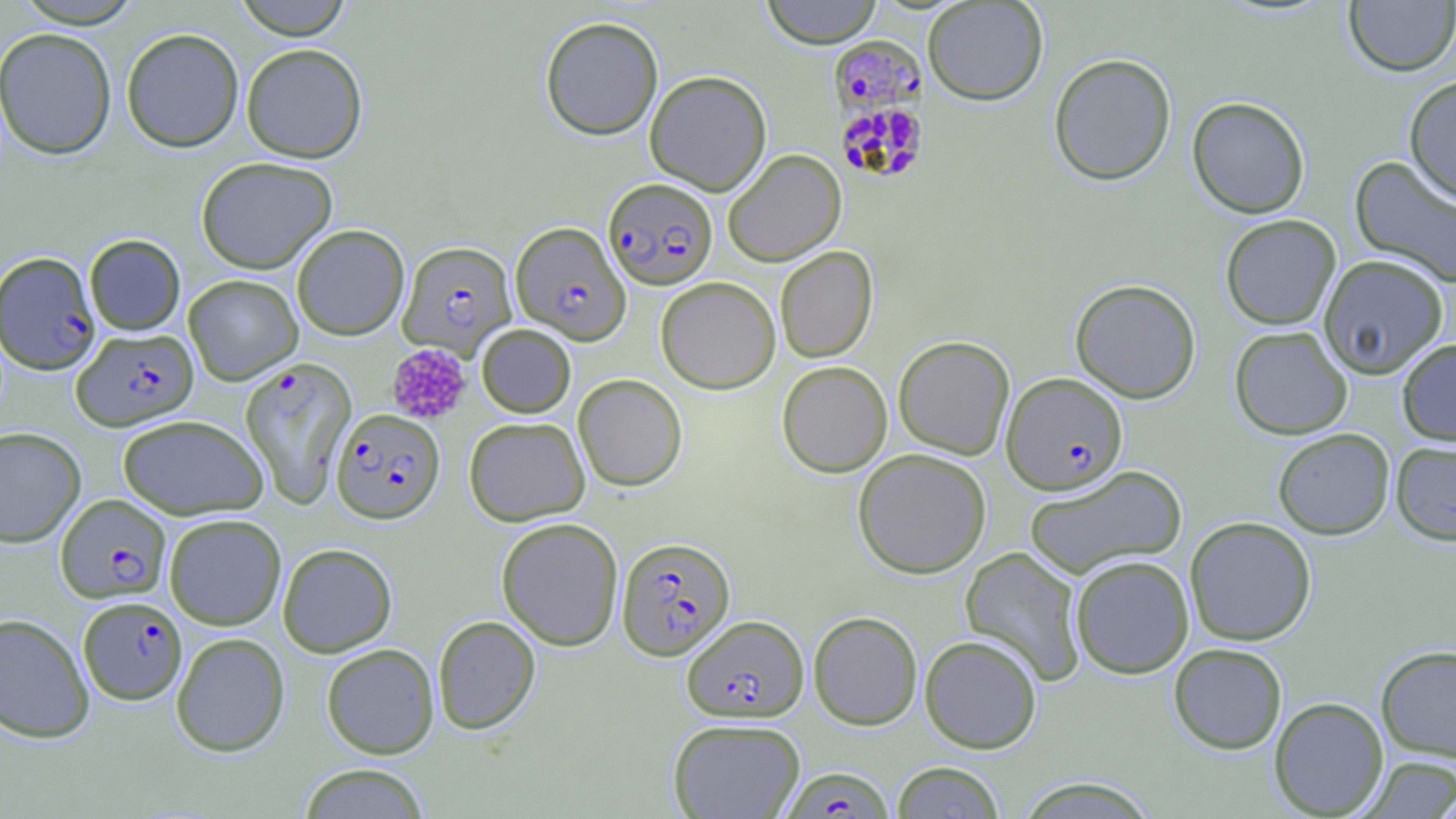

slide-level diagnosis = Plasmodium falciparum
stain = May-Grünwald-Giemsa
preparation = thin blood smear
uninfected red blood cell locations = approximate bounding boxes as (x1,y1)-(x2,y2) corner pairs in pixels: (10,0)-(145,28), (232,0)-(353,39), (761,0)-(883,48), (922,1)-(1048,105), (1344,1)-(1456,76), (540,16)-(663,141), (0,27)-(117,159), (121,27)-(244,152), (241,43)-(367,162), (1048,52)-(1176,186), (645,70)-(771,195), (1404,75)-(1456,204), (1187,96)-(1310,218), (723,150)-(846,267), (1350,155)-(1456,288), (196,156)-(338,274), (1220,214)-(1341,329), (292,224)-(409,340), (84,234)-(185,335), (775,246)-(878,363), (1318,255)-(1449,378), (184,274)-(303,384), (655,277)-(781,394), (1070,278)-(1201,403), (476,324)-(576,417), (1229,326)-(1353,439), (893,335)-(1015,459), (1397,338)-(1456,446), (777,361)-(892,477), (573,374)-(687,491), (118,414)-(268,520), (464,417)-(590,526), (0,427)-(86,547), (1273,428)-(1395,539), (1391,441)-(1456,546), (853,448)-(992,578), (1024,465)-(1188,580), (164,513)-(286,630), (1185,516)-(1316,646), (496,517)-(623,650), (278,543)-(397,657), (961,547)-(1086,685), (1070,555)-(1194,678), (809,611)-(922,730), (0,613)-(94,743), (432,615)-(540,734), (171,632)-(290,756), (919,634)-(1042,753), (321,643)-(439,759), (1169,643)-(1287,754), (1376,645)-(1456,763), (1269,697)-(1388,817), (668,718)-(805,818), (1359,755)-(1456,817), (892,762)-(1005,819), (298,764)-(430,819), (1014,777)-(1160,818)
magnification = 1000x
Plasmodium falciparum-infected red blood cell locations = approximate bounding boxes as (x1,y1)-(x2,y2) corner pairs in pixels: (828,36)-(926,127), (835,100)-(929,185), (604,178)-(718,290), (511,222)-(630,344), (398,241)-(517,359), (0,252)-(101,374), (72,328)-(198,430), (240,357)-(357,507), (1001,372)-(1127,494), (332,408)-(445,523), (56,494)-(171,603), (617,536)-(735,660), (78,596)-(187,704), (682,614)-(808,722), (782,767)-(894,818)
image size = 1456×819 pixels
field of view = one of a larger specimen
modality = optical microscopy
platelet locations = approximate bounding boxes as (x1,y1)-(x2,y2) corner pairs in pixels: (386,343)-(472,425)